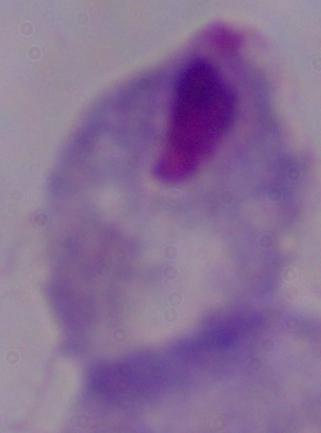

Captured at 1000x magnification. Photomicrograph. A trichomonad is shown.